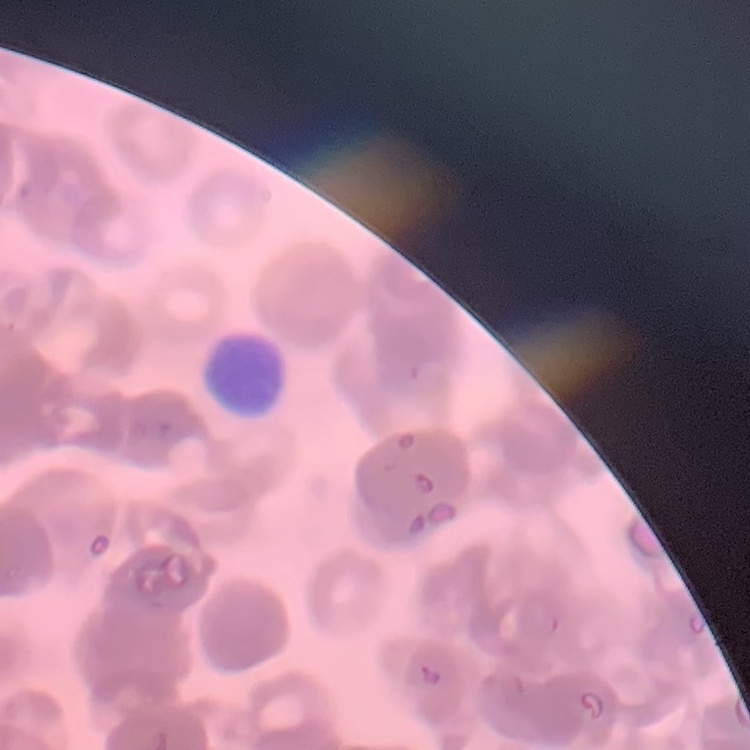 The erythrocytes show rouleaux formation. Stained with either Field's or Giemsa. Square crop of a larger photomicrograph. Thin blood film.